State the blood parasite species.
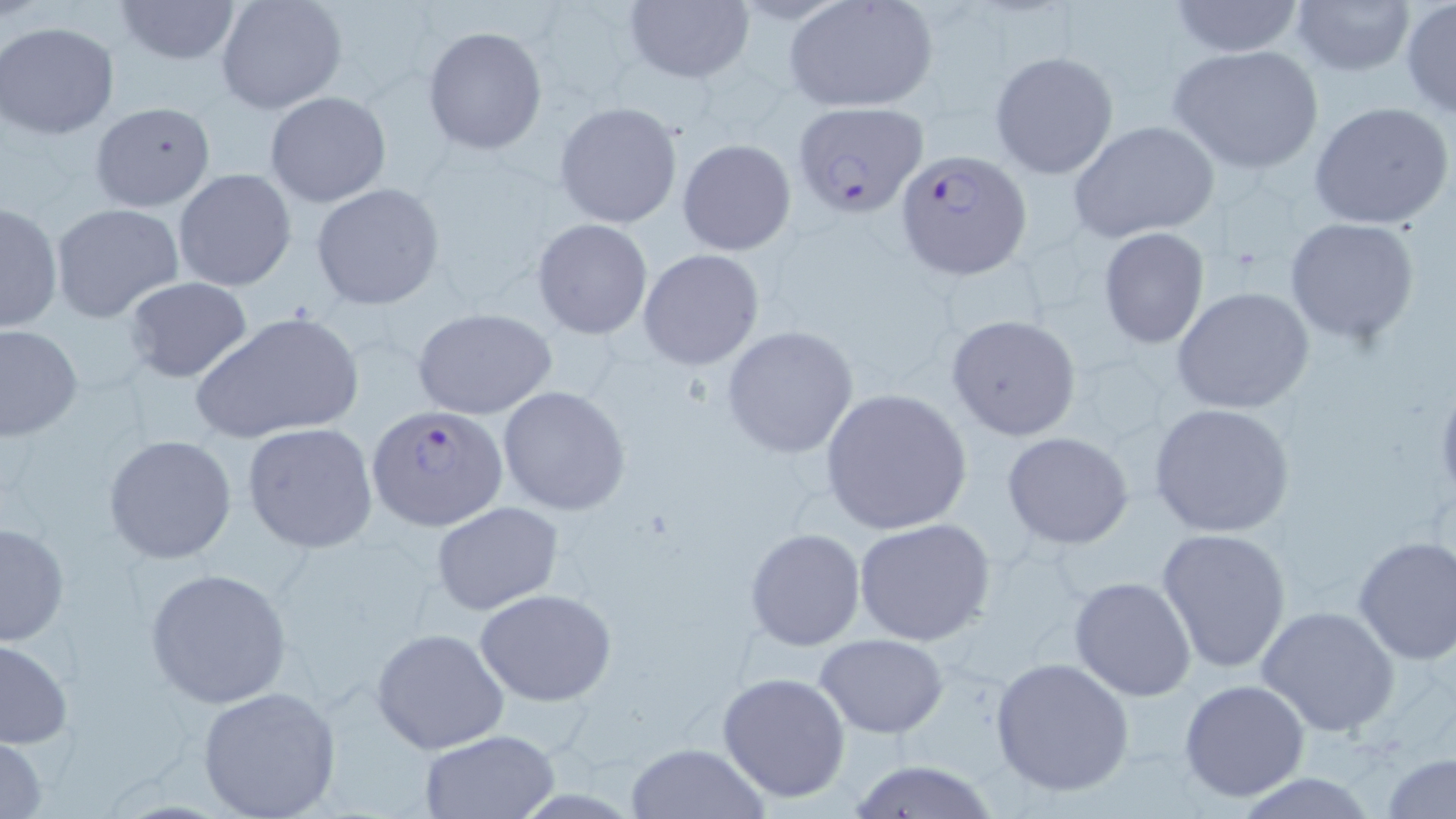

Plasmodium falciparum.

stain = May-Grünwald-Giemsa
preparation = thin blood smear
magnification = 1000x
uninfected red blood cell locations = approximate bounding boxes as [x1, y1, x2, y2] in pixels: [111, 0, 243, 64], [215, 0, 347, 114], [1289, 0, 1417, 76], [620, 1, 754, 87], [783, 1, 940, 111], [1165, 1, 1307, 58], [1401, 1, 1456, 119], [1, 22, 121, 139], [422, 26, 547, 155], [1168, 44, 1325, 174], [988, 50, 1119, 179], [265, 92, 391, 208], [90, 101, 216, 211], [555, 101, 683, 230], [1309, 101, 1456, 232], [1068, 121, 1221, 244], [676, 137, 797, 256], [174, 168, 296, 291], [310, 183, 445, 310], [0, 200, 63, 333], [51, 201, 185, 323], [1282, 217, 1422, 344], [532, 219, 652, 338], [1097, 227, 1210, 350], [636, 248, 766, 371], [123, 276, 253, 383], [1171, 286, 1315, 415], [413, 309, 557, 421], [190, 311, 365, 446], [944, 313, 1080, 441], [1, 323, 82, 443], [720, 325, 858, 459], [1431, 377, 1456, 507], [497, 384, 632, 516], [820, 388, 972, 535], [1149, 402, 1297, 538], [242, 422, 378, 553], [1002, 430, 1134, 549], [103, 434, 237, 564], [431, 501, 564, 614], [855, 519, 998, 648], [0, 521, 70, 646], [744, 527, 866, 651], [1156, 527, 1293, 672], [1350, 534, 1456, 667], [145, 566, 295, 708], [1069, 576, 1197, 702], [474, 588, 616, 706], [1255, 604, 1399, 736], [371, 627, 510, 755], [814, 634, 951, 738], [0, 637, 74, 748], [990, 656, 1134, 798], [718, 671, 851, 804], [1178, 679, 1311, 804], [196, 686, 342, 818], [417, 729, 559, 818], [0, 734, 50, 818], [624, 741, 769, 819], [1380, 751, 1455, 819], [842, 759, 1004, 817]
Plasmodium falciparum-infected red blood cell locations = approximate bounding boxes as [x1, y1, x2, y2] in pixels: [793, 102, 929, 216], [896, 150, 1029, 278], [366, 403, 507, 532]
modality = optical microscopy
field of view = single
image size = 1456×819 pixels